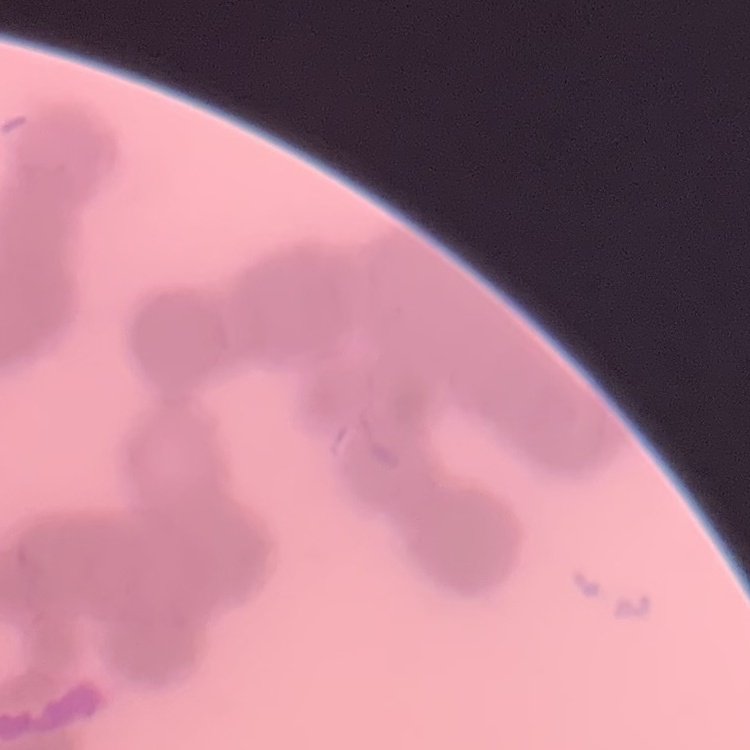
Summary:
  - Red blood cell morphology: rouleaux formation
  - Image type: square crop of a larger photomicrograph
  - Stain: Field's or Giemsa
  - Preparation: thin peripheral smear